Assess this cell for malaria.
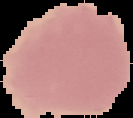

It is uninfected.

Image is 133×118 pixels. The area outside the segmented cell region is set to black. From a thin blood film.